Describe the morphology of the red blood cells.
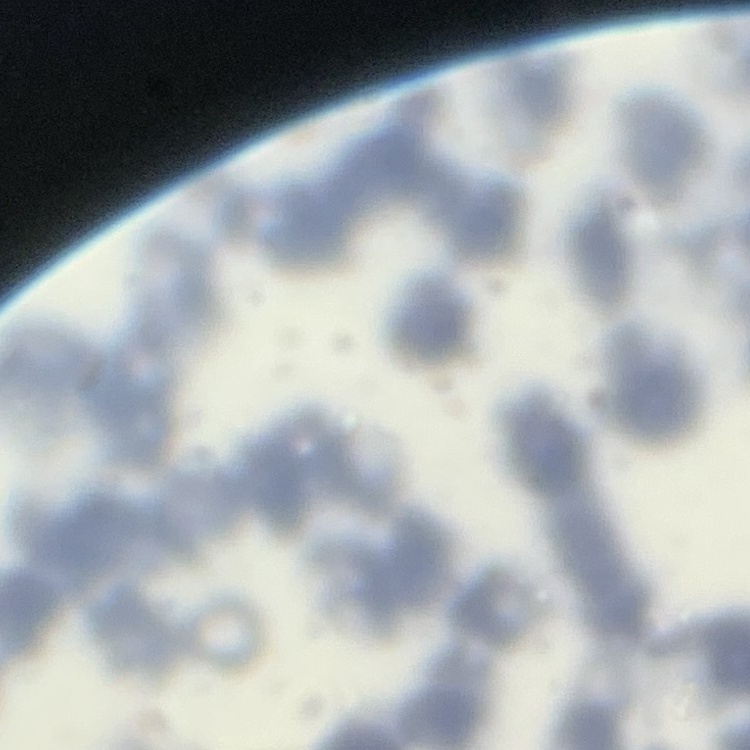
Rouleaux formation.

Thin peripheral smear. Field's or Giemsa stain. One tile cut from a larger photomicrograph.